Identify the cell.
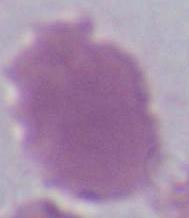

An erythrocyte.

Photomicrograph. 1000x magnification.